Identify the parasite.
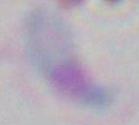
This is Toxoplasma gondii.

Summary:
  - Magnification: 1000x
  - Modality: photomicrograph